Assess the morphology of the erythrocytes.
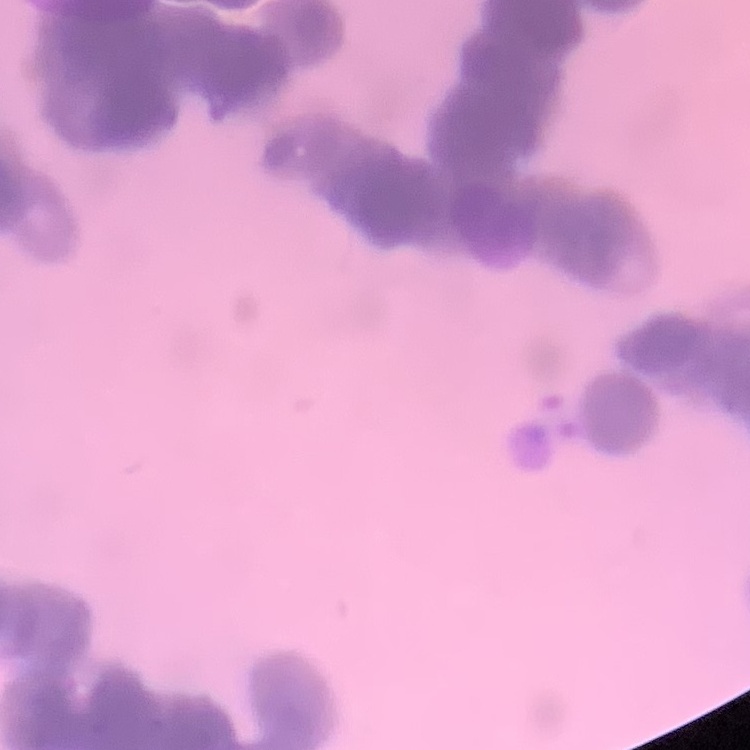
They show rouleaux formation.

Summary:
  - Preparation: thin blood film
  - Image type: square crop of a larger photomicrograph
  - Stain: Field's or Giemsa